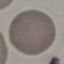
Malaria status: uninfected. Giemsa-stained preparation. Cell patch, automatically extracted from a larger field of view and resized to 64 × 64 pixels. Thin blood film. Photographed with a smartphone camera at the microscope eyepiece.